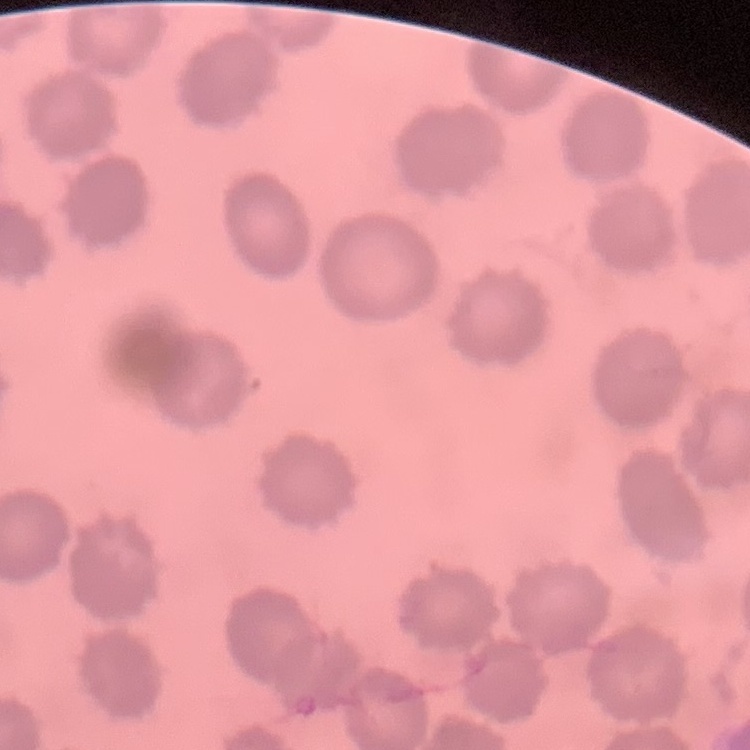 The red blood cells exhibit no rouleaux formation. Square crop of a larger photomicrograph. Stained with either Field's or Giemsa. Thin blood smear.